Describe the morphology of the red blood cells.
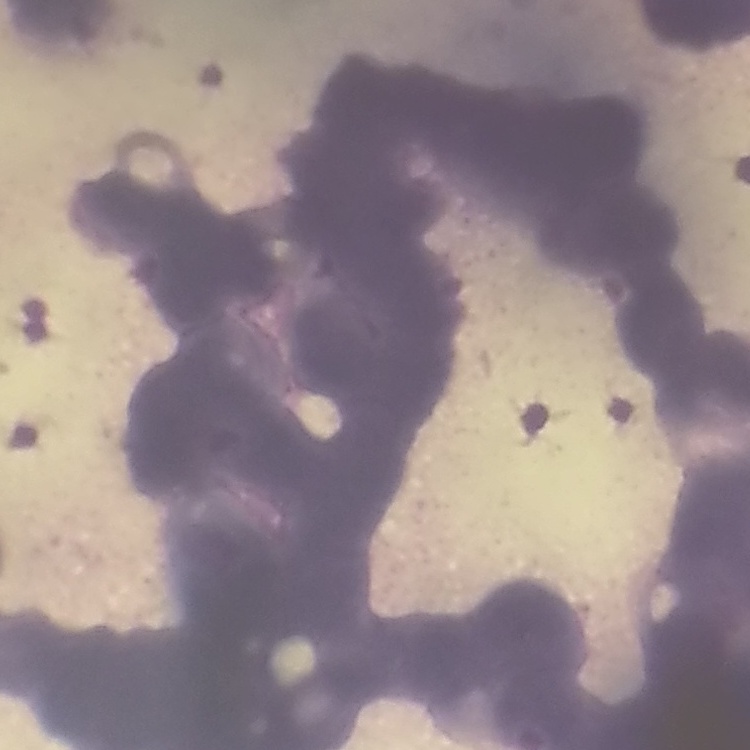
They show rouleaux formation.

Thin blood smear. Square crop of a larger photomicrograph. Field's or Giemsa stain.